Assess this cell for malaria.
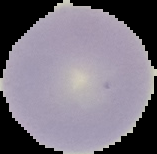
Uninfected.

From a thin blood film. Segmented cell region on a black background. Image is 157×154 pixels.